Classify this cell by malaria status.
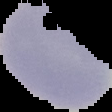
Uninfected.

image type = segmented cell region with the area outside set to black
preparation = thin blood smear
image size = 112×112 pixels